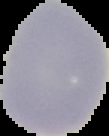
From a thin blood film. Result: no malaria parasites seen. Segmented cell region on a black background. Image is 109×136 pixels.